State which cell type is depicted.
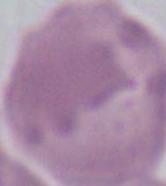
This is an erythrocyte.

magnification = 1000x
modality = micrograph